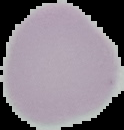
Result: negative for Plasmodium parasites. Segmented cell region on a black background. From a thin blood smear. Image is 124×130 pixels.